Locate every Plasmodium parasite and every leukocyte.
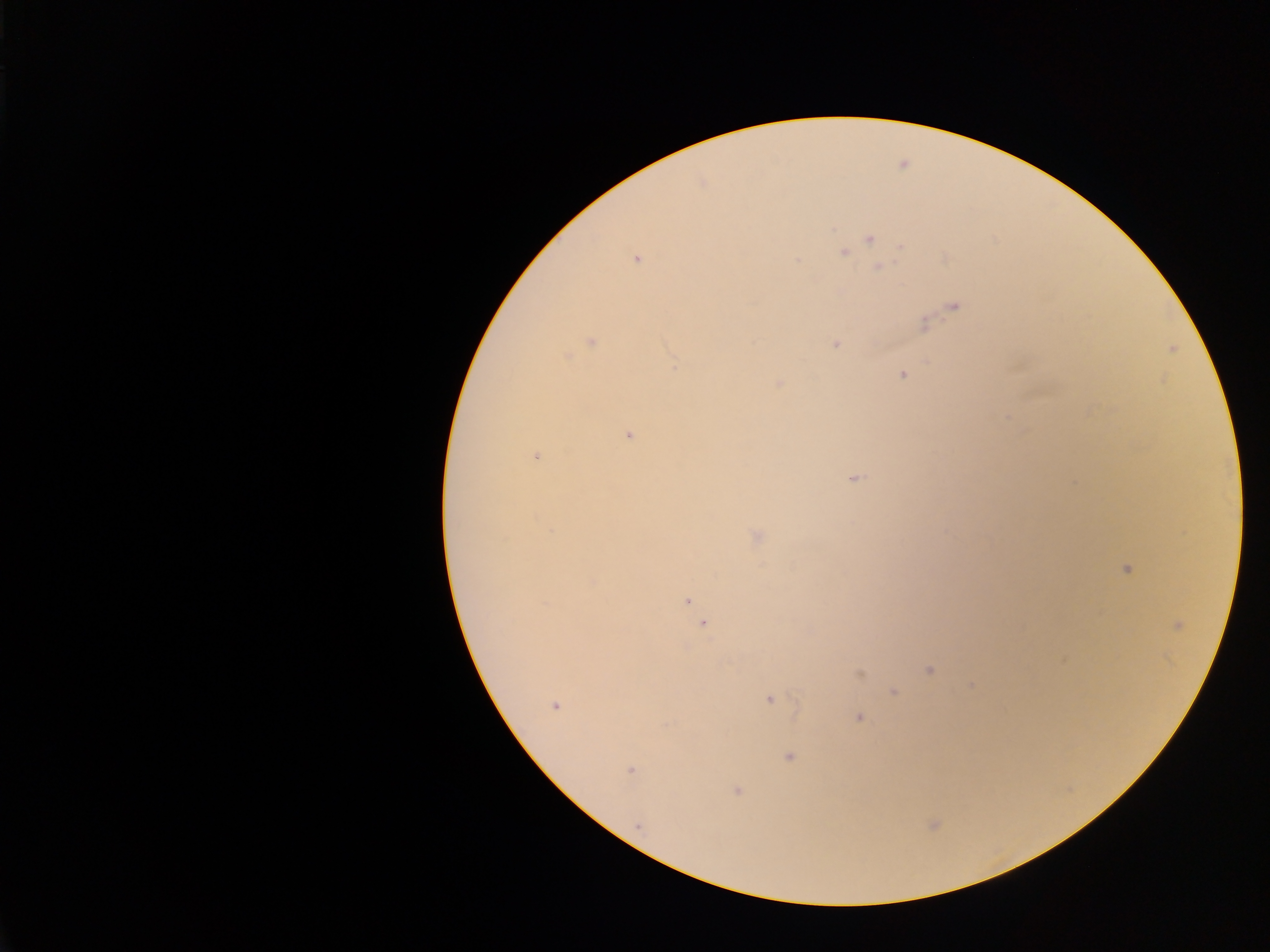
Approximate centers as [x, y] in pixels.
Plasmodium parasites: [832, 227], [868, 237], [844, 252], [798, 258], [637, 259], [878, 266], [954, 308], [924, 323], [591, 341], [835, 343], [565, 359], [925, 361], [674, 367], [901, 374], [780, 385], [629, 434], [537, 454], [853, 479], [755, 536], [1125, 569], [686, 601], [703, 624], [1062, 659], [928, 671], [858, 674], [893, 691], [769, 700], [556, 707], [795, 710], [858, 717], [788, 756], [631, 768], [738, 790].
No leukocytes observed.

{
  "capture": "mobile-phone photograph through a microscope",
  "field_of_view": "single",
  "preparation": "thick blood film",
  "image_size": "1270×952 pixels",
  "country": "Ghana"
}